Classify this cell by malaria status.
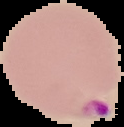
It is parasitized.

Cell region segmented out of the field of view; the surrounding area is masked to black. Image is 124×127 pixels. From a thin blood smear.